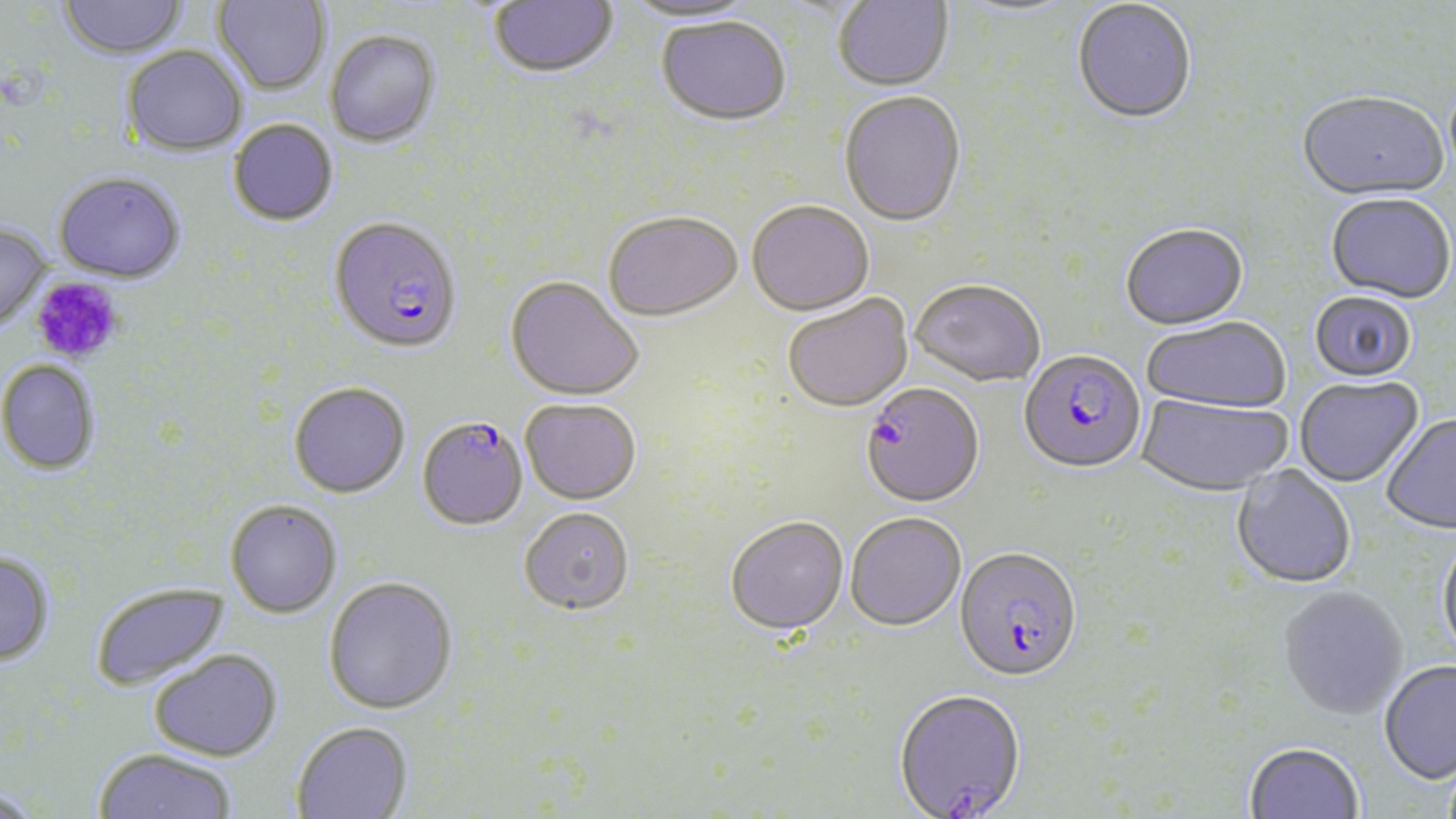

Summary:
  - Coordinate format: approximate bounding boxes as (x1,y1)-(x2,y2) corner pairs in pixels
  - Platelet locations: (30,277)-(124,364)
  - Plasmodium falciparum-infected red blood cell locations: (329,218)-(462,355), (1018,351)-(1146,477), (860,385)-(985,511), (417,416)-(528,531), (954,550)-(1083,685), (893,691)-(1027,819)
  - Uninfected red blood cell locations: (57,0)-(188,60), (212,0)-(330,96), (488,0)-(620,81), (833,0)-(953,93), (623,1)-(762,28), (951,1)-(1080,21), (1072,1)-(1197,127), (656,19)-(792,129), (325,29)-(440,146), (121,45)-(248,156), (839,93)-(966,230), (1297,93)-(1449,205), (228,118)-(339,226), (54,173)-(186,284), (1325,196)-(1455,306), (747,203)-(874,319), (604,214)-(743,324), (0,224)-(52,332), (1120,225)-(1249,333), (505,279)-(642,403), (910,281)-(1045,389), (1309,292)-(1416,385), (783,296)-(914,414), (1142,319)-(1291,415), (0,361)-(100,476), (1294,378)-(1424,489), (289,382)-(410,498), (1135,395)-(1292,499), (520,401)-(641,507), (1381,416)-(1456,536), (1231,465)-(1356,591), (226,500)-(342,617), (519,510)-(634,618), (846,515)-(966,634), (725,518)-(848,639), (1437,537)-(1456,662), (0,553)-(56,667), (323,577)-(459,716), (91,581)-(229,692), (1277,587)-(1409,722), (149,649)-(283,762), (1378,662)-(1456,786), (291,722)-(413,818), (1244,744)-(1364,819), (93,749)-(236,819), (0,789)-(44,819)
  - Slide-level diagnosis: Plasmodium falciparum
  - Field of view: one of a larger specimen
  - Preparation: thin blood smear
  - Magnification: 1000x
  - Modality: light microscopy
  - Stain: May-Grünwald-Giemsa
  - Image size: 1456×819 pixels